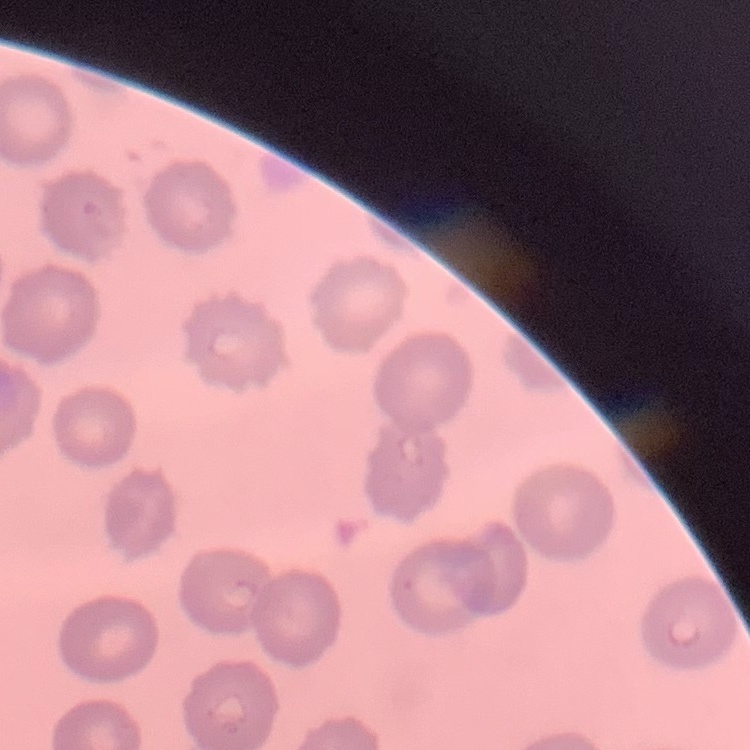
Summary:
  - Red blood cell morphology: no rouleaux formation
  - Image type: one tile cut from a larger photomicrograph
  - Preparation: thin blood smear
  - Stain: Field's or Giemsa